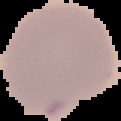

preparation = thin blood smear
image size = 121×121 pixels
result = no Plasmodium parasites seen
image type = cell region segmented out of the field of view; surrounding area masked to black